Identify the preparation type.
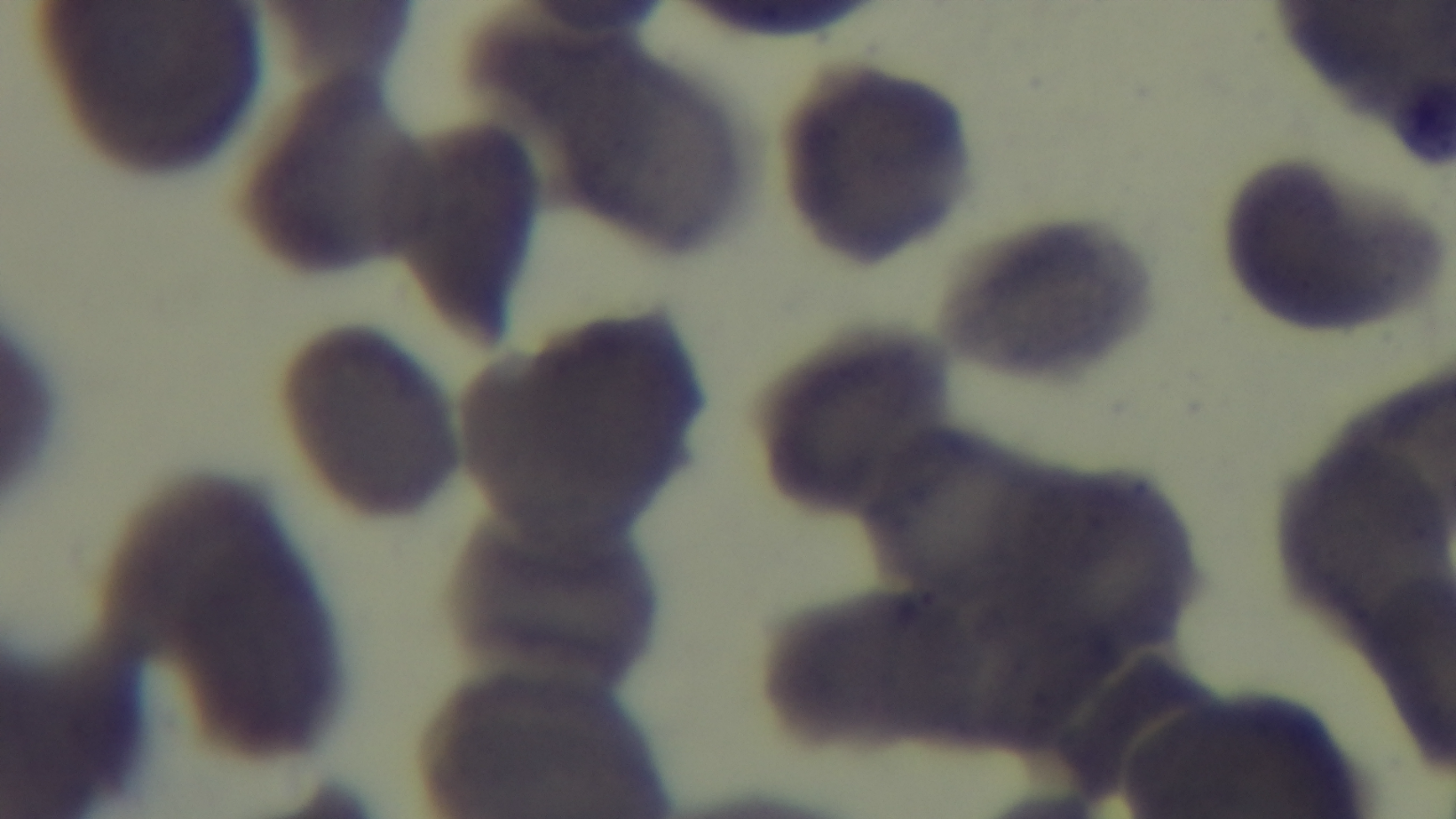
Thin.

Giemsa stain. Malaria status: uninfected. Photomicrograph. Single field of view. Oil-immersion objective, 100x. Mounted 4K digital camera.